Name the blood parasite species.
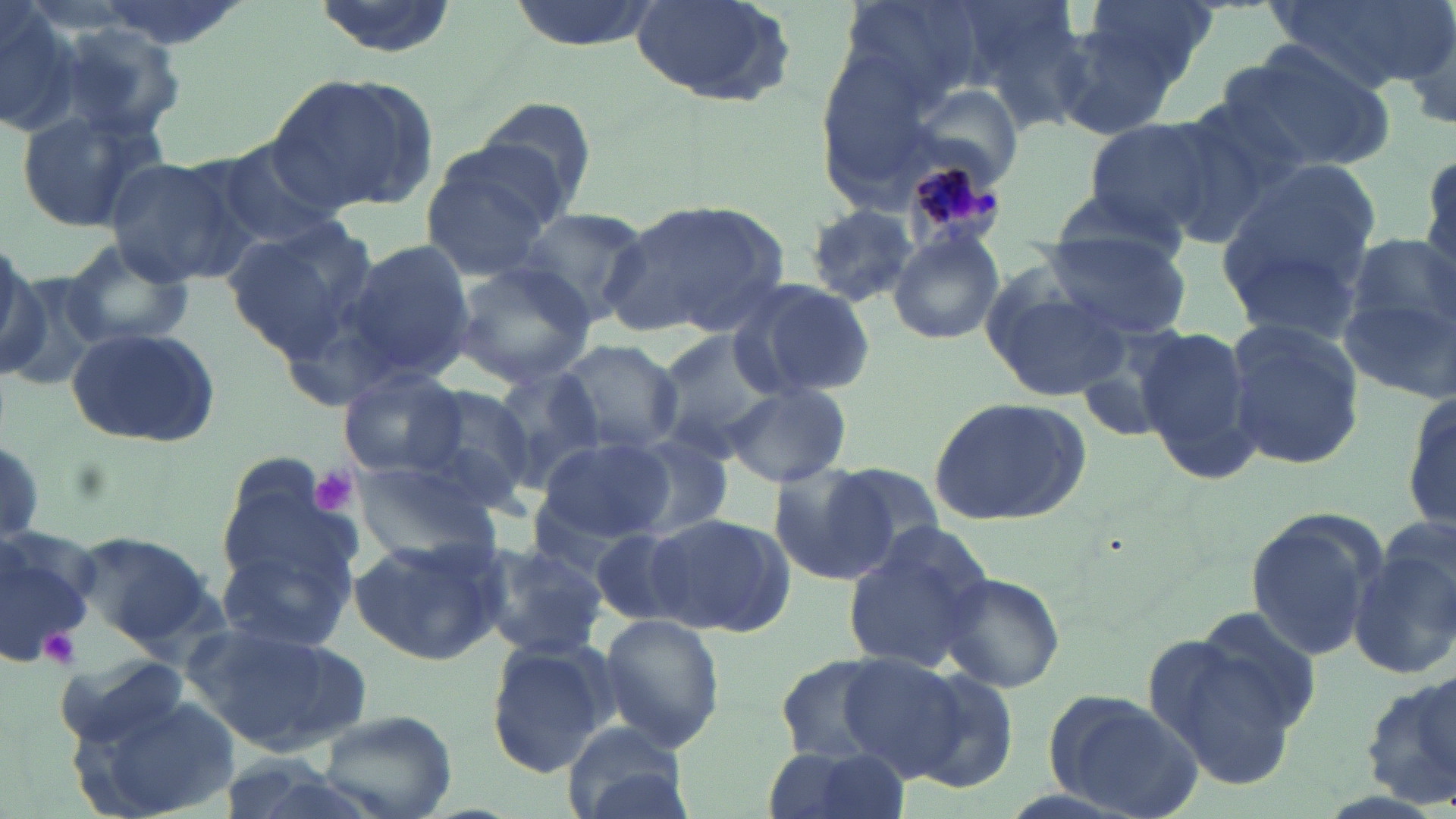

Plasmodium malariae.

modality: light microscopy
stain: May-Grünwald-Giemsa
plasmodium_malariae_infected_red_blood_cell_locations: 'approximate bounding boxes as [x1, y1, x2, y2] in pixels: [884, 137, 1004, 256]'
platelet_locations: 'approximate bounding boxes as [x1, y1, x2, y2] in pixels: [307, 465, 359, 517], [36, 627, 84, 669]'
field_of_view: one of a larger specimen
image_size: 1456×819 pixels
uninfected_red_blood_cell_locations: 'approximate bounding boxes as [x1, y1, x2, y2] in pixels: [0, 0, 83, 139], [89, 0, 251, 49], [305, 0, 461, 59], [501, 0, 670, 53], [628, 0, 798, 107], [1081, 0, 1219, 87], [1268, 0, 1447, 95], [1395, 14, 1456, 133], [1049, 17, 1190, 141], [51, 20, 188, 139], [1208, 43, 1396, 173], [268, 74, 438, 214], [474, 95, 599, 212], [1154, 105, 1301, 244], [16, 106, 171, 235], [1081, 117, 1221, 235], [209, 138, 346, 250], [418, 139, 565, 278], [1418, 145, 1455, 282], [101, 155, 250, 284], [1215, 162, 1382, 327], [1044, 180, 1194, 259], [605, 197, 793, 338], [801, 202, 921, 307], [513, 209, 649, 323], [221, 218, 377, 356], [887, 232, 1005, 347], [1040, 233, 1192, 341], [1340, 238, 1456, 394], [334, 239, 476, 388], [59, 241, 195, 351], [0, 256, 70, 390], [448, 260, 599, 389], [979, 269, 1135, 406], [722, 276, 876, 401], [1226, 319, 1365, 471], [65, 324, 224, 449], [1133, 328, 1262, 486], [648, 330, 783, 460], [555, 338, 685, 458], [338, 367, 469, 479], [488, 367, 606, 490], [1401, 379, 1456, 540], [417, 383, 544, 503], [725, 384, 850, 486], [926, 396, 1091, 526], [615, 433, 735, 540], [534, 436, 672, 545], [354, 459, 500, 559], [215, 460, 362, 626], [821, 461, 948, 572], [766, 466, 892, 586], [1244, 508, 1388, 663], [647, 512, 792, 637], [588, 523, 703, 626], [1, 524, 102, 664], [835, 525, 993, 676], [70, 531, 216, 648], [348, 534, 506, 668], [474, 540, 609, 662], [1349, 543, 1456, 682], [217, 545, 353, 653], [937, 571, 1065, 694], [1191, 607, 1323, 733], [597, 612, 726, 753], [184, 618, 374, 757], [1141, 630, 1310, 793], [486, 639, 613, 776], [54, 654, 192, 751], [834, 654, 973, 779], [773, 655, 904, 762], [896, 668, 1019, 795], [1362, 674, 1456, 810], [1041, 690, 1204, 819], [69, 692, 246, 819], [317, 709, 457, 819], [561, 722, 690, 819], [757, 745, 908, 819]'
magnification: 1000x
preparation: thin blood film